Locate every blood parasite and identify its species.
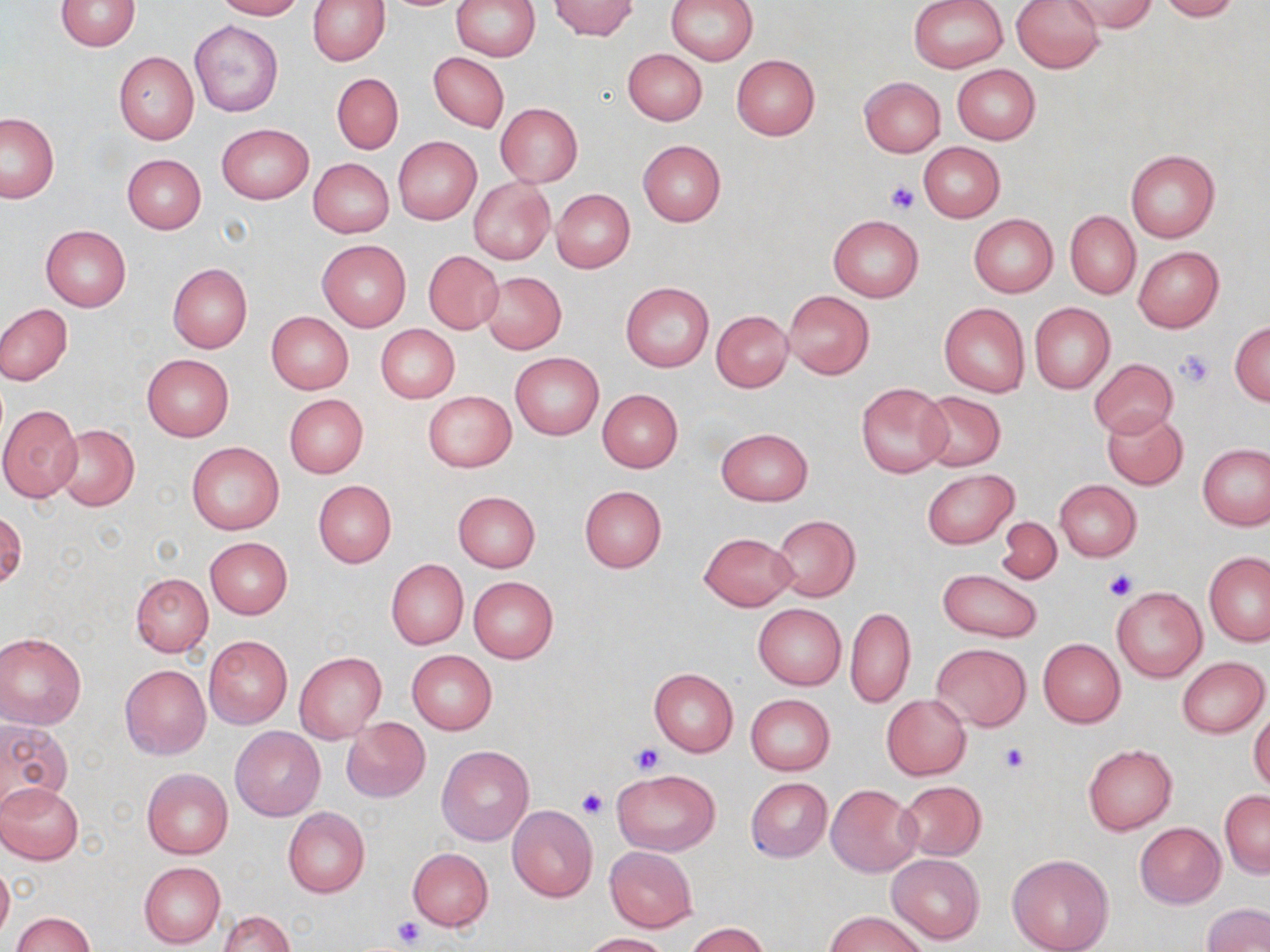
No blood parasites observed.

Approximate bounding boxes as (x1,y1)-(x2,y2) corner pairs in pixels. Platelet locations: (885,182)-(919,214), (1176,349)-(1214,388), (1105,571)-(1137,600), (631,742)-(664,775), (999,742)-(1029,774), (576,789)-(608,820), (393,915)-(426,948). Uninfected red blood cell locations: (55,0)-(142,50), (213,0)-(302,20), (307,0)-(391,65), (451,0)-(540,61), (550,0)-(637,41), (667,0)-(758,64), (909,0)-(1008,73), (1011,0)-(1104,73), (1066,0)-(1158,34), (1157,0)-(1240,21), (189,19)-(285,117), (622,48)-(708,126), (115,52)-(198,144), (428,53)-(509,132), (731,54)-(820,139), (952,64)-(1040,145), (331,73)-(403,154), (858,77)-(945,157), (496,103)-(582,187), (0,113)-(58,202), (216,123)-(313,203), (393,136)-(481,224), (637,140)-(726,227), (918,142)-(1005,222), (1125,148)-(1220,242), (122,153)-(205,234), (309,158)-(394,238), (469,178)-(554,264), (550,188)-(635,273), (1066,210)-(1140,299), (828,214)-(923,302), (969,214)-(1058,298), (41,225)-(131,311), (317,240)-(411,331), (1133,245)-(1223,333), (422,250)-(503,334), (167,263)-(252,353), (481,271)-(567,354), (621,282)-(714,372), (783,291)-(874,379), (939,303)-(1030,397), (1029,303)-(1115,393), (0,304)-(73,385), (711,310)-(792,391), (266,312)-(354,393), (1230,321)-(1270,405), (376,324)-(459,403), (511,352)-(603,440), (143,354)-(233,440), (1089,358)-(1178,438), (856,382)-(951,478), (597,389)-(682,473), (423,391)-(516,472), (916,392)-(1005,472), (284,394)-(367,478), (0,403)-(83,503), (1102,408)-(1187,489), (53,424)-(139,512), (715,427)-(814,506), (186,441)-(285,534), (1198,442)-(1270,530), (922,468)-(1018,548), (313,480)-(396,568), (1055,480)-(1142,561), (579,484)-(667,573), (453,491)-(540,571), (0,509)-(25,591), (771,514)-(860,602), (996,516)-(1061,585), (698,531)-(797,610), (204,536)-(293,618), (1204,552)-(1270,646), (385,559)-(468,649), (936,568)-(1043,643), (130,573)-(213,657), (468,576)-(558,663), (1112,586)-(1207,681), (753,603)-(846,690), (846,606)-(915,708), (0,633)-(86,730), (204,636)-(293,730), (1038,638)-(1125,727), (931,643)-(1031,731), (407,650)-(496,734), (294,652)-(388,744), (1178,657)-(1269,738), (119,665)-(210,759), (648,667)-(738,756), (746,694)-(835,774), (882,694)-(971,780), (1249,709)-(1270,791), (0,717)-(72,813), (342,718)-(429,802), (231,726)-(326,821), (1083,744)-(1177,834), (437,745)-(535,846), (612,767)-(721,856), (141,768)-(232,858), (745,777)-(832,862), (896,780)-(987,860), (1,782)-(84,864), (826,783)-(922,877), (1220,789)-(1269,877), (507,805)-(598,901), (283,806)-(370,897), (1135,822)-(1225,908), (604,846)-(697,931), (407,848)-(493,930), (1006,852)-(1114,952), (887,853)-(984,944), (0,860)-(13,943), (138,862)-(225,949), (1203,903)-(1269,952), (217,911)-(295,952), (827,911)-(927,952), (10,912)-(96,952), (686,922)-(771,952), (580,932)-(674,952). Slide-level diagnosis: no evidence of blood parasites. One field of a larger specimen. Image is 1270×952 pixels. Optical microscopy. 1000x magnification. Thin blood film. May-Grünwald-Giemsa-stained preparation.